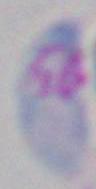

identification = Toxoplasma gondii
magnification = 1000x
modality = photomicrograph